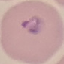

malaria status = parasitized
preparation = thin blood smear
image type = automatically extracted cell patch, resized to 64 × 64 pixels
capture = smartphone through the microscope eyepiece
stain = Giemsa